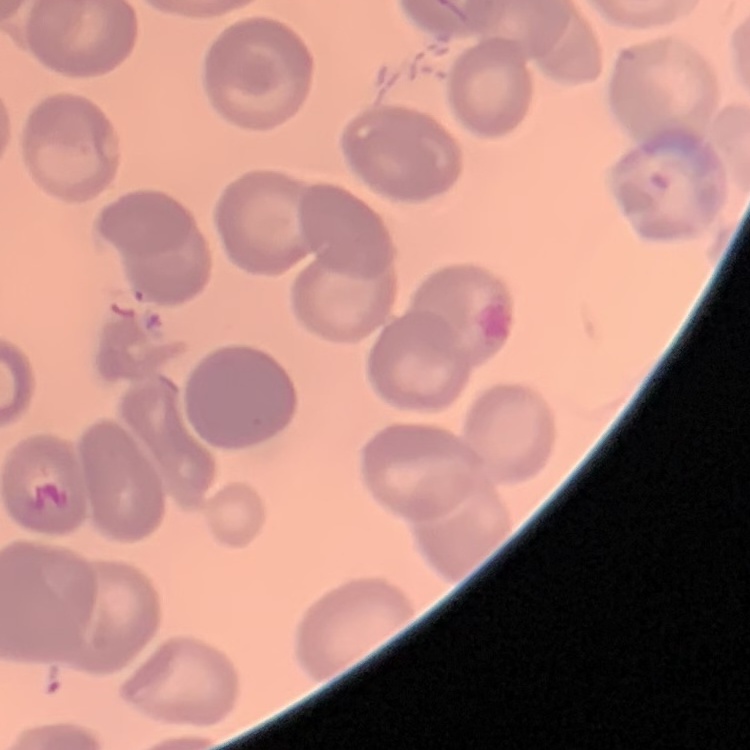

Summary:
  - Erythrocyte morphology: no rouleaux formation
  - Preparation: thin peripheral smear
  - Stain: Field's or Giemsa
  - Image type: one tile cut from a larger photomicrograph